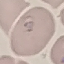
result = malaria parasites identified
preparation = thin smear
stain = Giemsa
capture = smartphone camera at the microscope eyepiece
image type = cell patch, automatically extracted from a larger field of view and resized to 64 × 64 pixels